Identify the parasite.
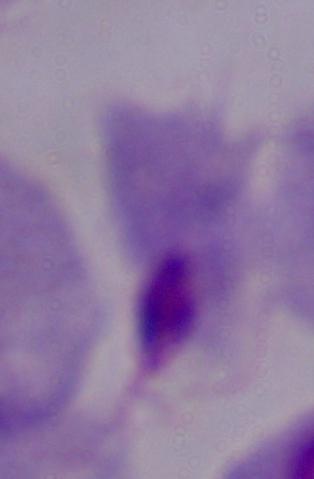
A trichomonad.

Captured at 1000x magnification. Micrograph.